Locate every malaria parasite.
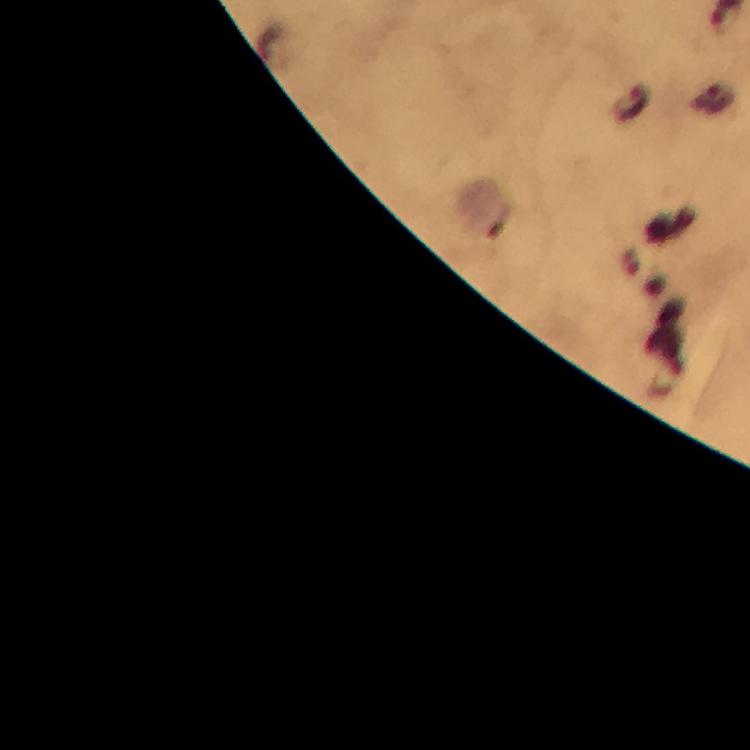
Approximate centers as [x, y] in pixels.
Malaria parasites: [714, 98], [631, 104].

Immersion oil applied. Image is 750×750 pixels. Smartphone photograph taken through a microscope. Giemsa stain. At 100x magnification. From a diagnostic examination for malaria. Cropped region of a single field of view. Thick blood film.